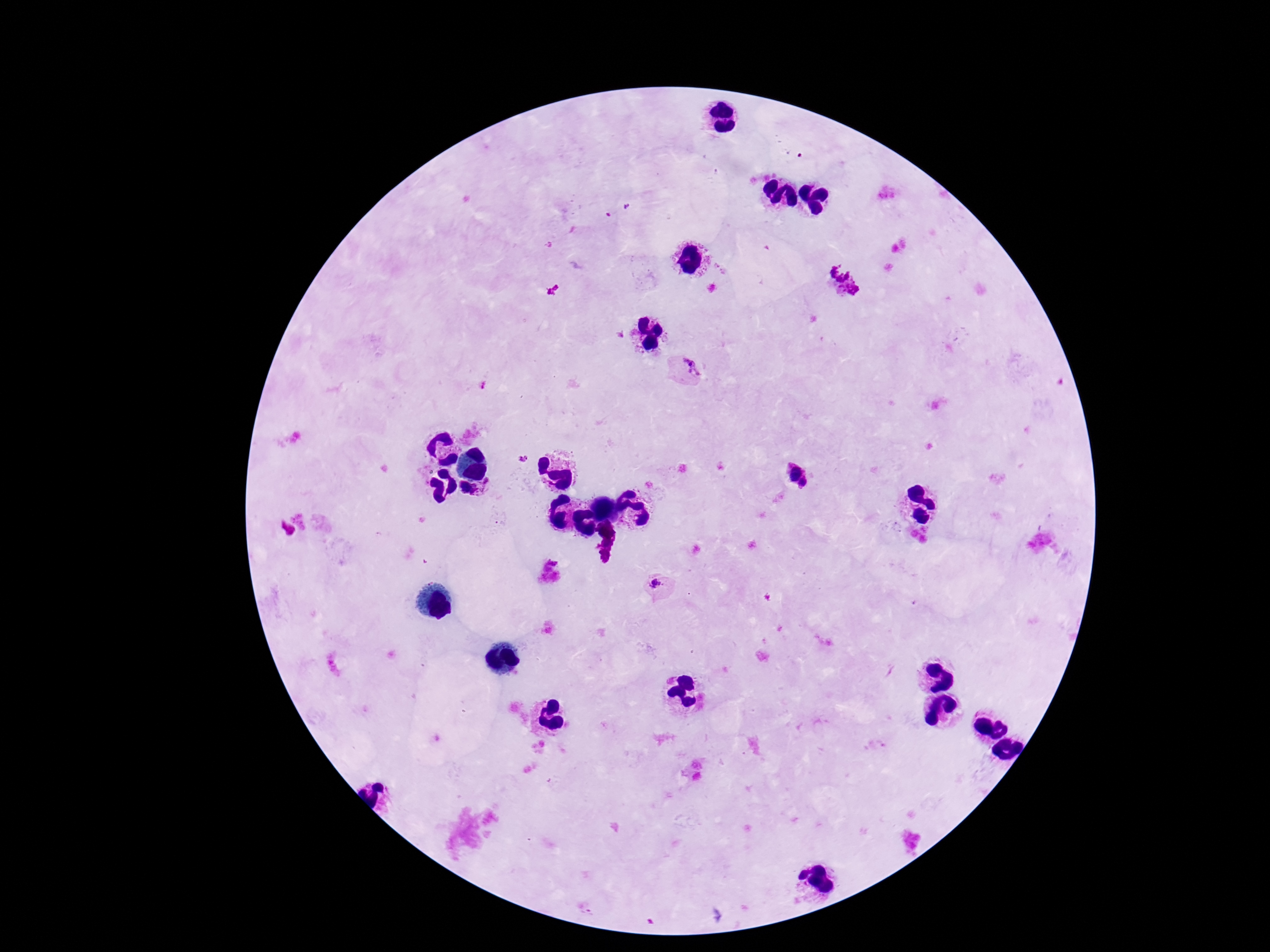

Approximate centers as {x, y} in pixels.
Summary:
  - Plasmodium parasite locations: {691, 366}, {523, 458}, {794, 471}, {489, 484}, {804, 484}, {469, 490}, {657, 583}
  - Stain: Giemsa
  - Patient malaria status: positive
  - Magnification: 100x
  - Preparation: thick blood film
  - Capture: smartphone camera through the microscope eyepiece
  - Field of view: one from this slide
  - Image size: 1270×952 pixels